Classify this cell by malaria status.
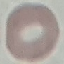

Uninfected.

Cell patch, automatically extracted from a larger field of view and resized to 64 × 64 pixels. Photographed with a smartphone camera at the microscope eyepiece. Giemsa-stained preparation. Thin blood smear.